Assess this cell for malaria.
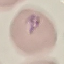

It is parasitized.

{
  "image_type": "cell patch, automatically extracted from a larger field of view and resized to 64 × 64 pixels",
  "preparation": "thin blood film",
  "stain": "Giemsa",
  "capture": "smartphone through the microscope eyepiece"
}